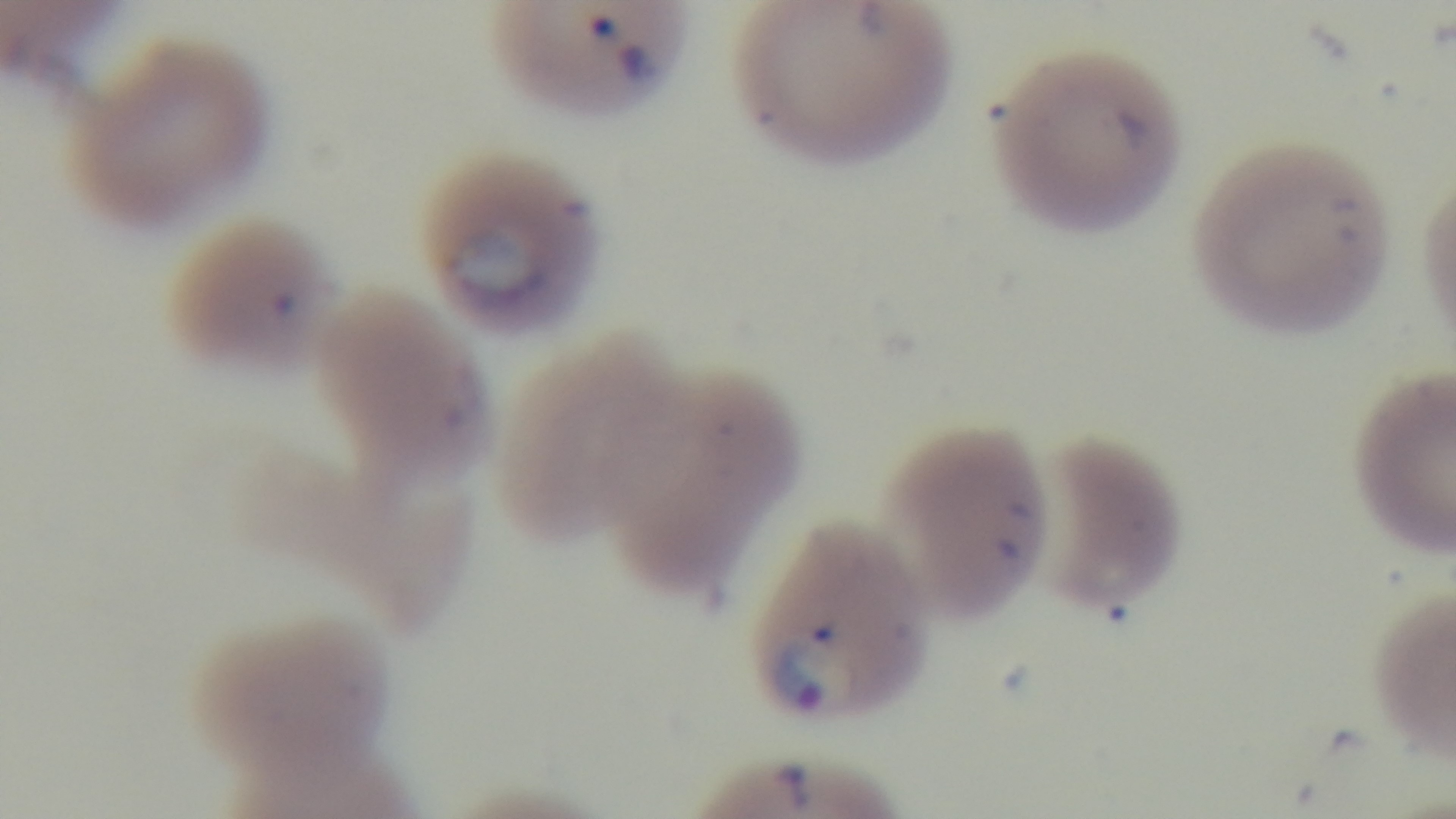
Captured with a mounted 4K digital camera. Preparation: thin. Oil-immersion objective, 100x. Photomicrograph. Malaria status: positive. Giemsa stain. One field from the slide.